Report the malaria status of this cell.
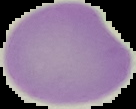

Uninfected.

{
  "preparation": "thin blood smear",
  "image_type": "cell region segmented out of the field of view; surrounding area masked to black",
  "image_size": "136×109 pixels"
}